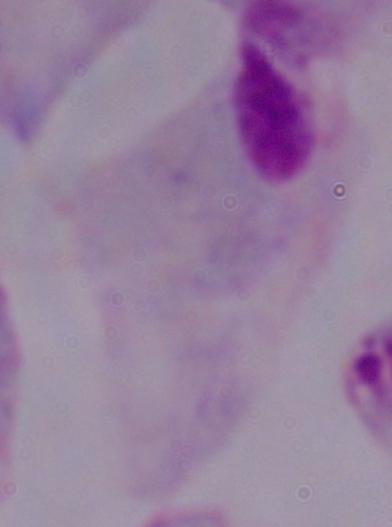 A trichomonad is shown. 1000x magnification. Photomicrograph.